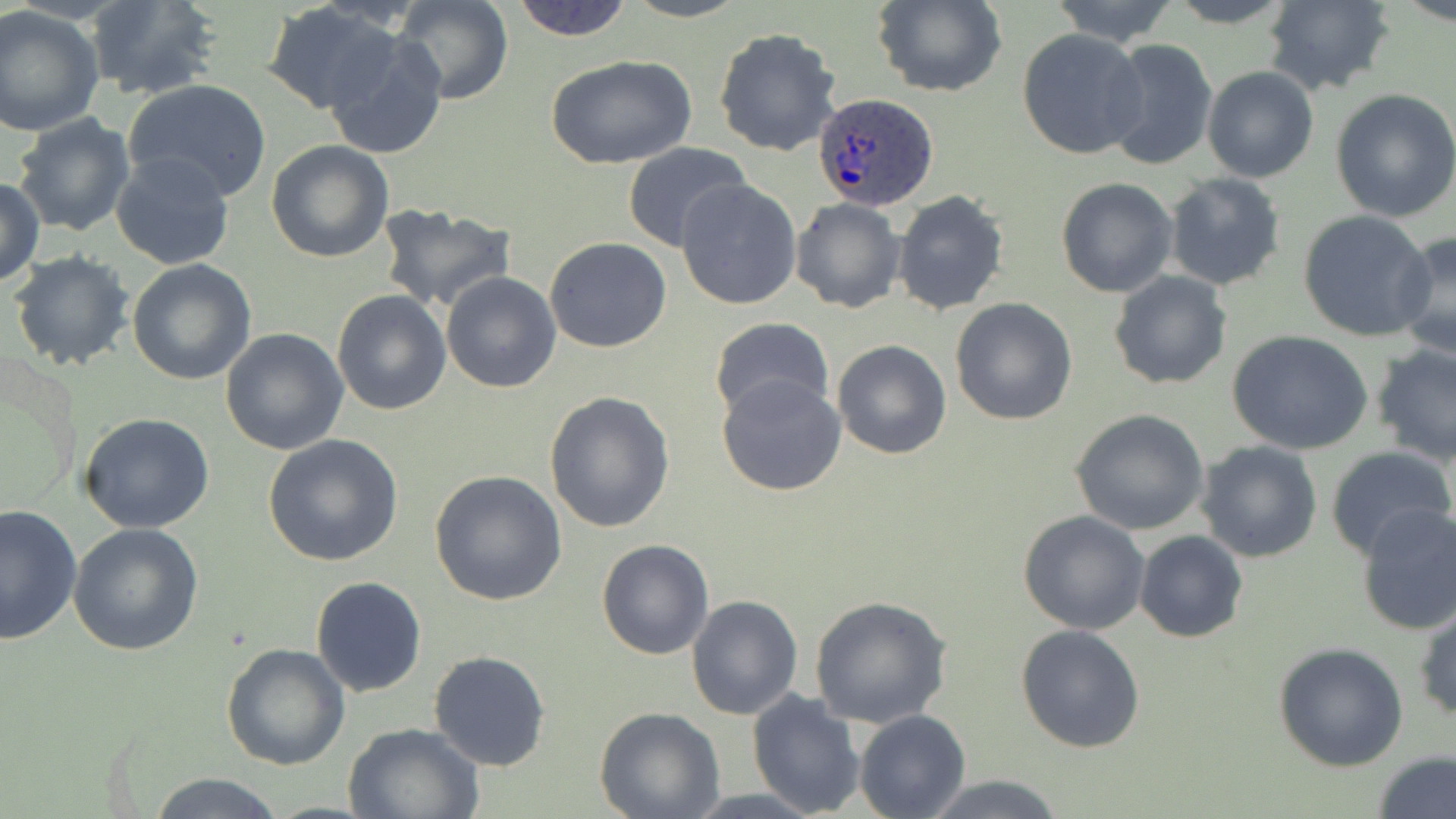
slide-level diagnosis = Plasmodium ovale
stain = May-Grünwald-Giemsa
preparation = thin blood film
modality = optical microscopy
field of view = single
image size = 1456×819 pixels
uninfected red blood cell locations = approximate bounding boxes as named x1/y1/x2/y2 corners in pixels: (x1=83, y1=0, x2=221, y2=100), (x1=393, y1=0, x2=513, y2=104), (x1=509, y1=0, x2=636, y2=41), (x1=622, y1=0, x2=750, y2=23), (x1=1048, y1=0, x2=1183, y2=48), (x1=1160, y1=0, x2=1302, y2=28), (x1=1261, y1=0, x2=1395, y2=95), (x1=870, y1=1, x2=1007, y2=97), (x1=263, y1=3, x2=402, y2=115), (x1=0, y1=6, x2=104, y2=137), (x1=712, y1=27, x2=842, y2=157), (x1=1017, y1=28, x2=1148, y2=159), (x1=324, y1=33, x2=449, y2=158), (x1=1100, y1=37, x2=1218, y2=173), (x1=545, y1=53, x2=697, y2=168), (x1=1202, y1=66, x2=1319, y2=183), (x1=125, y1=79, x2=272, y2=200), (x1=1330, y1=89, x2=1456, y2=223), (x1=11, y1=112, x2=136, y2=238), (x1=266, y1=141, x2=394, y2=263), (x1=621, y1=144, x2=753, y2=253), (x1=110, y1=150, x2=237, y2=272), (x1=1164, y1=173, x2=1286, y2=290), (x1=0, y1=177, x2=46, y2=289), (x1=675, y1=178, x2=802, y2=309), (x1=1056, y1=178, x2=1179, y2=298), (x1=893, y1=190, x2=1009, y2=317), (x1=789, y1=197, x2=905, y2=314), (x1=374, y1=204, x2=519, y2=313), (x1=1297, y1=210, x2=1435, y2=342), (x1=1391, y1=229, x2=1456, y2=360), (x1=544, y1=237, x2=672, y2=353), (x1=10, y1=252, x2=135, y2=372), (x1=127, y1=260, x2=257, y2=386), (x1=1108, y1=269, x2=1233, y2=390), (x1=442, y1=271, x2=562, y2=393), (x1=332, y1=290, x2=451, y2=414), (x1=949, y1=298, x2=1078, y2=425), (x1=709, y1=317, x2=834, y2=423), (x1=220, y1=329, x2=349, y2=456), (x1=1228, y1=331, x2=1374, y2=457), (x1=832, y1=340, x2=953, y2=459), (x1=1371, y1=343, x2=1456, y2=465), (x1=717, y1=374, x2=847, y2=496), (x1=543, y1=390, x2=675, y2=533), (x1=1071, y1=408, x2=1210, y2=535), (x1=80, y1=413, x2=216, y2=533), (x1=262, y1=434, x2=405, y2=566), (x1=1197, y1=440, x2=1323, y2=564), (x1=1326, y1=446, x2=1456, y2=561), (x1=428, y1=471, x2=568, y2=608), (x1=1354, y1=502, x2=1456, y2=636), (x1=0, y1=503, x2=82, y2=643), (x1=1017, y1=510, x2=1150, y2=633), (x1=68, y1=521, x2=203, y2=656), (x1=1135, y1=530, x2=1248, y2=644), (x1=596, y1=538, x2=714, y2=659), (x1=311, y1=575, x2=427, y2=697), (x1=809, y1=594, x2=954, y2=728), (x1=686, y1=595, x2=804, y2=720), (x1=1413, y1=605, x2=1456, y2=722), (x1=1016, y1=625, x2=1145, y2=752), (x1=1272, y1=642, x2=1408, y2=770), (x1=221, y1=643, x2=350, y2=770), (x1=428, y1=650, x2=552, y2=771), (x1=746, y1=691, x2=867, y2=818), (x1=595, y1=707, x2=725, y2=819), (x1=855, y1=709, x2=970, y2=819), (x1=342, y1=722, x2=485, y2=818), (x1=1374, y1=753, x2=1456, y2=819), (x1=147, y1=772, x2=285, y2=818), (x1=920, y1=774, x2=1068, y2=817)
Plasmodium ovale-infected red blood cell locations = approximate bounding boxes as named x1/y1/x2/y2 corners in pixels: (x1=813, y1=92, x2=941, y2=210)
magnification = 1000x